Outline each uninfected red blood cell.
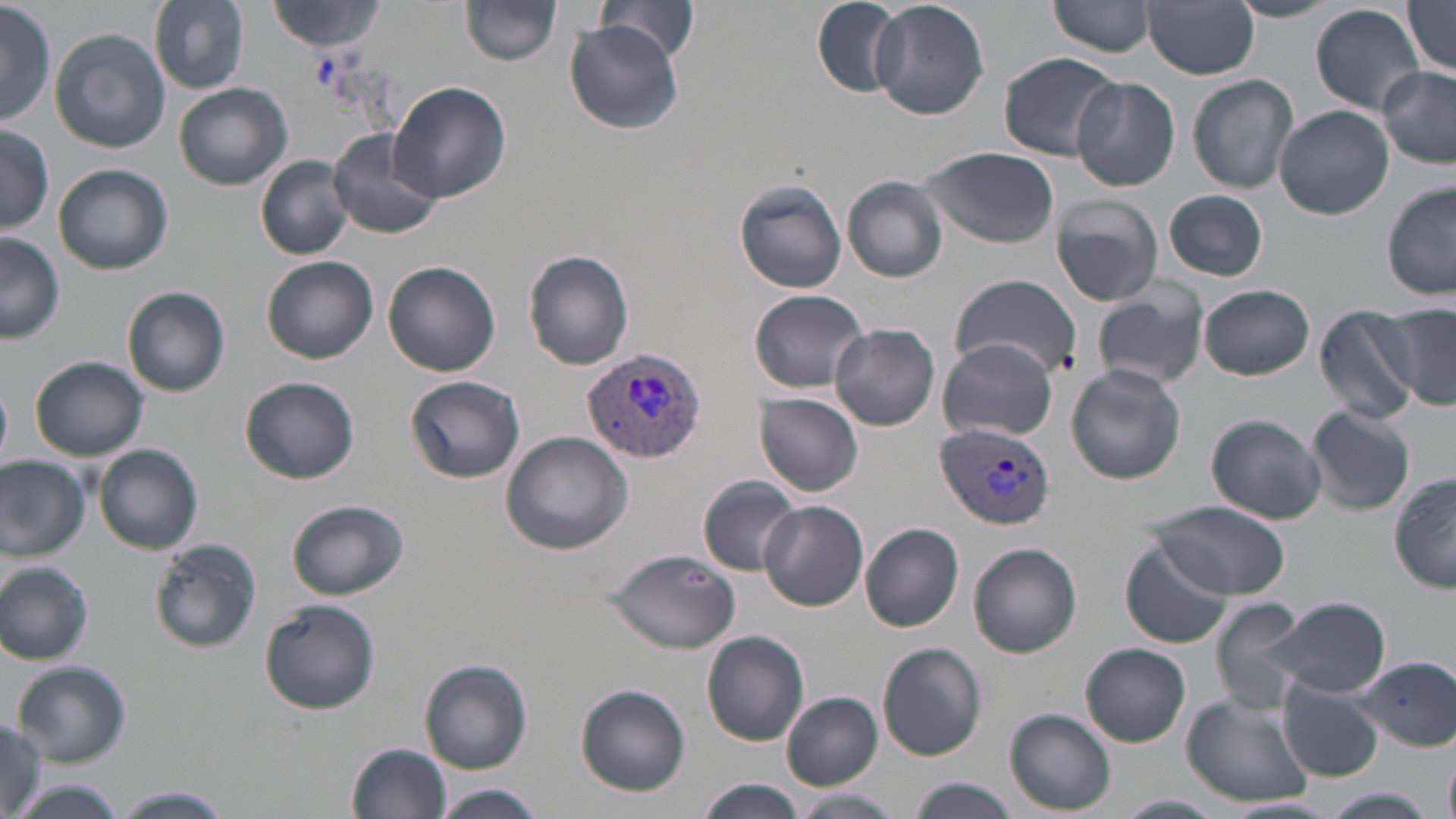

Approximate bounding boxes as named x1/y1/x2/y2 corners in pixels.
Uninfected red blood cells: (x1=1, y1=0, x2=55, y2=129), (x1=152, y1=0, x2=248, y2=91), (x1=808, y1=0, x2=907, y2=97), (x1=870, y1=0, x2=989, y2=120), (x1=1049, y1=0, x2=1160, y2=58), (x1=1228, y1=0, x2=1339, y2=22), (x1=268, y1=1, x2=388, y2=52), (x1=1144, y1=1, x2=1260, y2=78), (x1=1401, y1=1, x2=1456, y2=74), (x1=464, y1=2, x2=564, y2=67), (x1=597, y1=2, x2=699, y2=61), (x1=1311, y1=3, x2=1423, y2=113), (x1=565, y1=21, x2=681, y2=133), (x1=50, y1=27, x2=171, y2=153), (x1=1000, y1=51, x2=1121, y2=161), (x1=1378, y1=64, x2=1456, y2=168), (x1=1189, y1=74, x2=1299, y2=193), (x1=1071, y1=77, x2=1180, y2=190), (x1=387, y1=81, x2=511, y2=205), (x1=174, y1=82, x2=292, y2=190), (x1=1275, y1=105, x2=1394, y2=220), (x1=0, y1=123, x2=54, y2=234), (x1=327, y1=127, x2=444, y2=241), (x1=921, y1=147, x2=1059, y2=249), (x1=256, y1=157, x2=354, y2=259), (x1=53, y1=165, x2=173, y2=275), (x1=844, y1=177, x2=948, y2=282), (x1=734, y1=180, x2=845, y2=293), (x1=1383, y1=180, x2=1456, y2=302), (x1=1162, y1=189, x2=1269, y2=281), (x1=1051, y1=195, x2=1165, y2=307), (x1=0, y1=234, x2=65, y2=343), (x1=524, y1=250, x2=635, y2=370), (x1=263, y1=256, x2=379, y2=364), (x1=384, y1=261, x2=500, y2=377), (x1=950, y1=272, x2=1081, y2=381), (x1=1199, y1=285, x2=1315, y2=380), (x1=123, y1=286, x2=231, y2=396), (x1=1092, y1=286, x2=1209, y2=390), (x1=748, y1=288, x2=871, y2=393), (x1=1314, y1=306, x2=1423, y2=424), (x1=1380, y1=307, x2=1456, y2=410), (x1=830, y1=323, x2=941, y2=430), (x1=937, y1=337, x2=1058, y2=443), (x1=30, y1=357, x2=149, y2=462), (x1=1066, y1=365, x2=1186, y2=484), (x1=407, y1=375, x2=526, y2=483), (x1=241, y1=376, x2=361, y2=485), (x1=756, y1=392, x2=864, y2=496), (x1=1306, y1=405, x2=1416, y2=515), (x1=1207, y1=414, x2=1326, y2=525), (x1=500, y1=431, x2=633, y2=555), (x1=92, y1=444, x2=203, y2=553), (x1=0, y1=453, x2=89, y2=560), (x1=1389, y1=470, x2=1455, y2=595), (x1=697, y1=476, x2=803, y2=577), (x1=286, y1=499, x2=409, y2=600), (x1=1155, y1=500, x2=1293, y2=598), (x1=759, y1=501, x2=868, y2=611), (x1=861, y1=523, x2=965, y2=632), (x1=151, y1=539, x2=260, y2=652), (x1=1120, y1=540, x2=1231, y2=649), (x1=968, y1=544, x2=1081, y2=658), (x1=604, y1=548, x2=741, y2=654), (x1=0, y1=562, x2=94, y2=665), (x1=1268, y1=595, x2=1390, y2=700), (x1=1208, y1=596, x2=1312, y2=712), (x1=260, y1=599, x2=381, y2=715), (x1=701, y1=630, x2=809, y2=746), (x1=878, y1=643, x2=988, y2=761), (x1=1082, y1=643, x2=1191, y2=746), (x1=1353, y1=657, x2=1455, y2=748), (x1=420, y1=658, x2=533, y2=773), (x1=13, y1=660, x2=131, y2=766), (x1=576, y1=685, x2=691, y2=795), (x1=1278, y1=686, x2=1384, y2=781), (x1=782, y1=692, x2=883, y2=790), (x1=1181, y1=695, x2=1317, y2=808), (x1=1006, y1=709, x2=1116, y2=815), (x1=0, y1=717, x2=54, y2=819), (x1=349, y1=741, x2=454, y2=819), (x1=1443, y1=749, x2=1455, y2=819), (x1=907, y1=777, x2=1019, y2=819), (x1=698, y1=779, x2=808, y2=818), (x1=13, y1=780, x2=127, y2=819), (x1=434, y1=785, x2=545, y2=818), (x1=114, y1=787, x2=231, y2=819), (x1=1322, y1=789, x2=1436, y2=819), (x1=793, y1=790, x2=900, y2=816), (x1=1117, y1=793, x2=1224, y2=817).

slide_level_diagnosis: Plasmodium vivax
preparation: thin blood smear
modality: light microscopy
plasmodium_vivax_infected_red_blood_cell_locations: 'approximate bounding boxes as named x1/y1/x2/y2 corners in pixels: (x1=583, y1=348, x2=706, y2=462), (x1=936, y1=421, x2=1053, y2=532)'
stain: May-Grünwald-Giemsa
field_of_view: one of a larger specimen
image_size: 1456×819 pixels
magnification: 1000x